Classify this cell by malaria status.
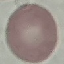
It is uninfected.

Cell patch, automatically extracted from a larger field of view and resized to 64 × 64 pixels. Acquired by smartphone through the microscope eyepiece. Giemsa stain. Thin blood smear.